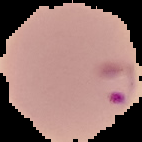

Summary:
  - Image type: segmented cell region with the area outside set to black
  - Malaria status: parasitized
  - Image size: 142×142 pixels
  - Preparation: thin blood smear